Assess the morphology of the erythrocytes.
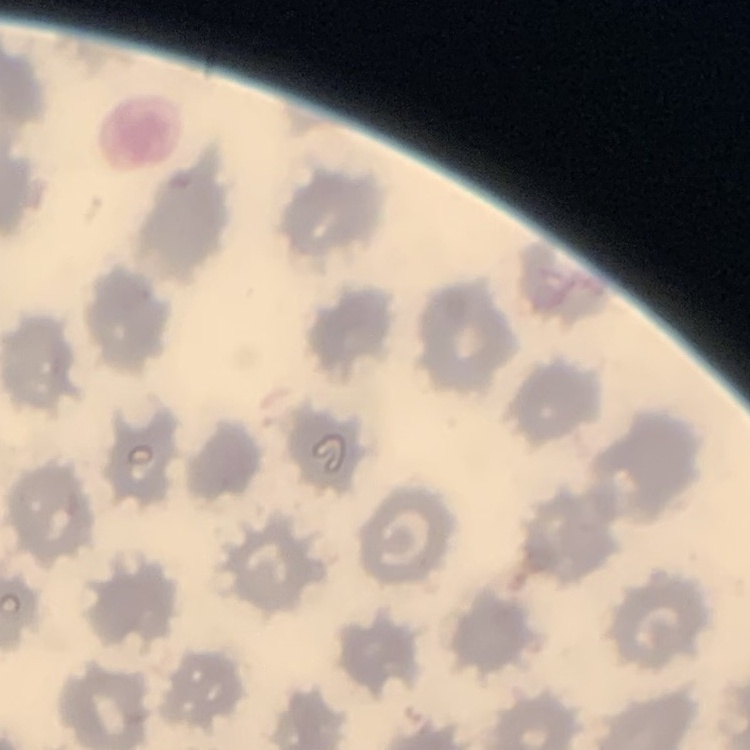
No rouleaux formation.

preparation = thin peripheral smear
image type = one tile cut from a larger photomicrograph
stain = Field's or Giemsa